Report the malaria status of this cell.
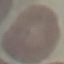
Uninfected.

stain = Giemsa
preparation = thin blood film
image type = cell patch, automatically extracted from a larger field of view and resized to 64 × 64 pixels
capture = smartphone through the microscope eyepiece